Outline each P. falciparum parasite and classify it by life-cycle stage.
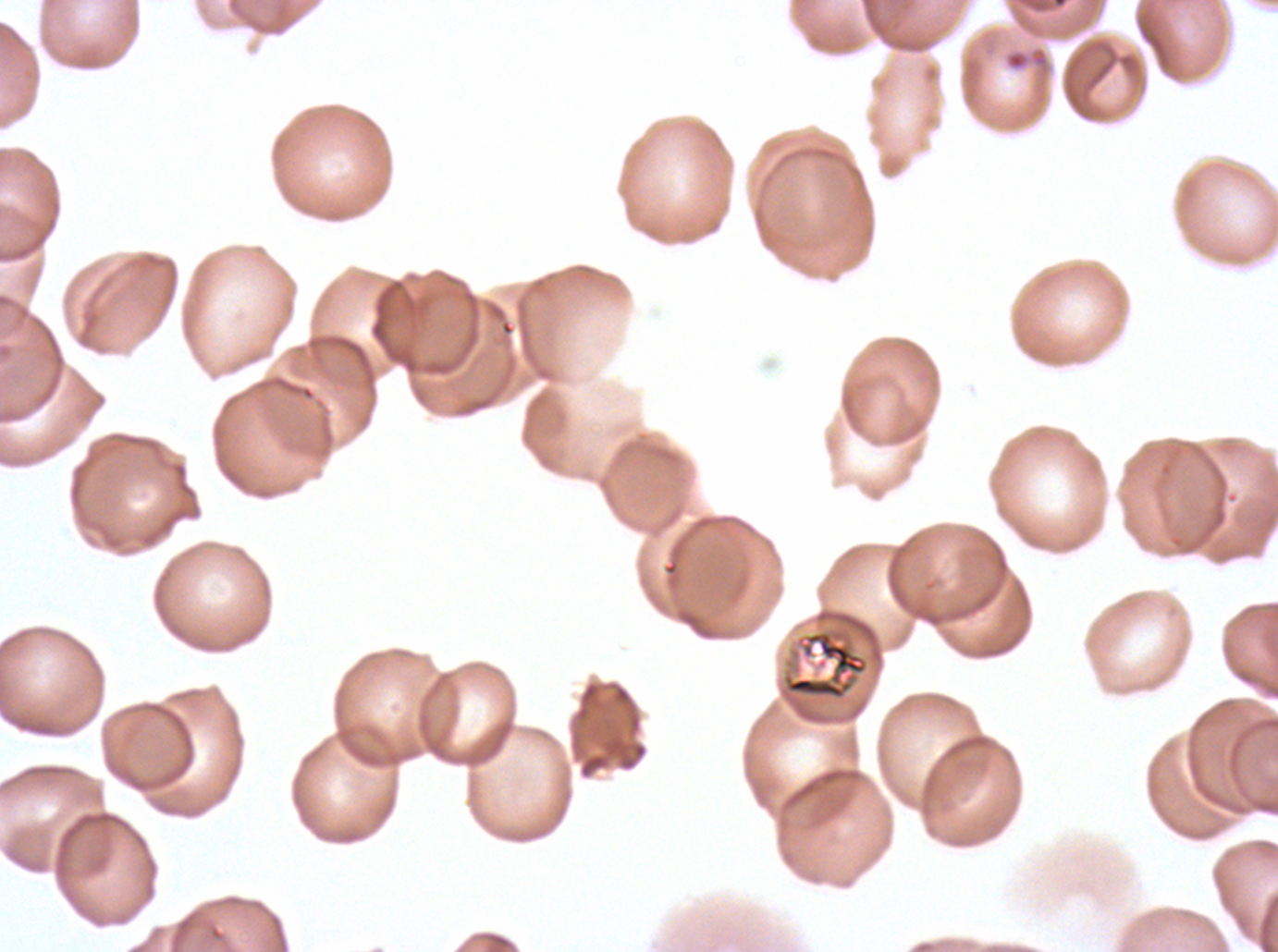
No rings, late-ring/early-trophozoite forms, mid trophozoites, late trophozoites, early schizonts, late schizonts, segmenters, or gametocytes observed.

notation = approximate bounding rectangles given as corner coordinates in pixels from the top-left
debris locations = (x1=1004, y1=46, x2=1051, y2=76), (x1=781, y1=629, x2=869, y2=701)
preparation = thin blood smear
field of view = one sub-image of a larger composite
stain = Giemsa
image size = 1278×952 pixels
specimen = P. falciparum cultured ex vivo for 24 to 48 hours, from a patient in The Gambia